Outline each uninfected red blood cell.
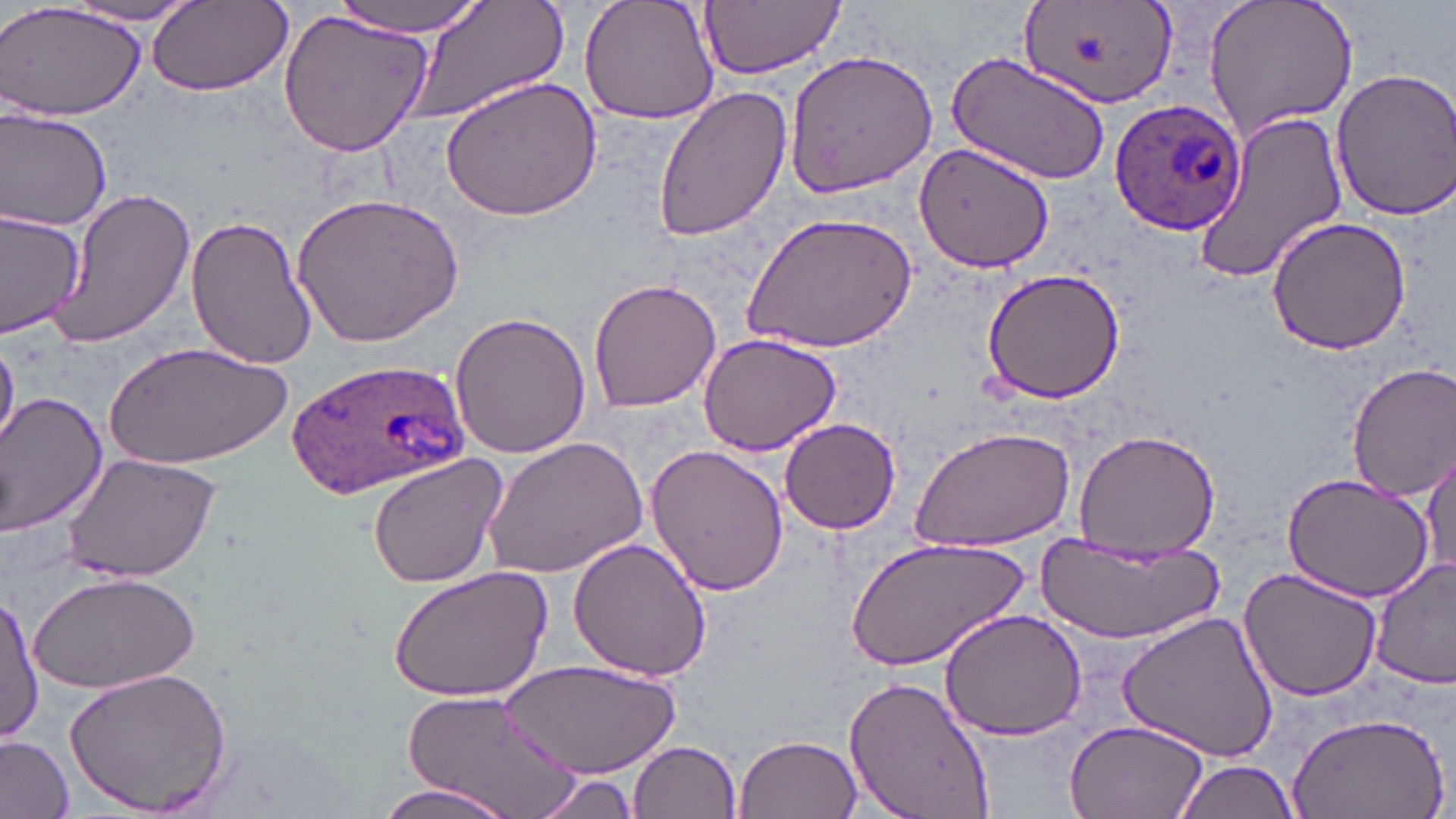
Approximate bounding boxes as (x1, y1, x2, y2) in pixels.
Uninfected red blood cells: (0, 0, 147, 120), (335, 0, 487, 34), (405, 0, 569, 123), (578, 0, 723, 124), (698, 0, 844, 79), (1202, 0, 1359, 141), (148, 1, 293, 98), (1016, 1, 1181, 113), (61, 2, 205, 27), (279, 8, 434, 160), (783, 49, 939, 197), (944, 51, 1112, 185), (1328, 65, 1456, 223), (438, 73, 603, 223), (652, 82, 793, 242), (0, 105, 114, 233), (1190, 110, 1349, 285), (918, 141, 1058, 272), (45, 188, 197, 349), (291, 189, 463, 347), (0, 207, 86, 337), (742, 213, 917, 356), (184, 214, 315, 369), (1266, 215, 1412, 358), (978, 266, 1126, 405), (588, 276, 724, 413), (449, 308, 590, 458), (697, 331, 843, 459), (0, 338, 19, 453), (107, 340, 293, 470), (1346, 363, 1456, 501), (0, 391, 108, 537), (778, 418, 903, 535), (910, 427, 1077, 554), (1072, 428, 1220, 556), (481, 437, 645, 580), (1422, 444, 1454, 582), (644, 445, 790, 598), (60, 451, 220, 585), (366, 454, 507, 590), (1280, 474, 1434, 605), (850, 534, 1027, 673), (1034, 535, 1224, 642), (567, 537, 714, 683), (1368, 558, 1456, 692), (387, 565, 553, 703), (1238, 567, 1383, 702), (30, 569, 201, 695), (1, 591, 41, 748), (938, 606, 1089, 740), (1118, 609, 1279, 765), (500, 660, 679, 777), (63, 665, 234, 816), (843, 674, 999, 819), (396, 687, 588, 818), (1286, 707, 1450, 819), (1061, 717, 1211, 819), (735, 732, 862, 819), (0, 734, 74, 818), (630, 740, 742, 819), (1172, 757, 1302, 819), (528, 769, 648, 819), (368, 780, 520, 819).

slide-level diagnosis = Plasmodium ovale
modality = optical microscopy
stain = May-Grünwald-Giemsa
Plasmodium ovale-infected red blood cell locations = approximate bounding boxes as (x1, y1, x2, y2) in pixels: (1109, 100, 1245, 240), (283, 355, 472, 498)
magnification = 1000x
image size = 1456×819 pixels
preparation = thin blood smear
field of view = one of a larger specimen